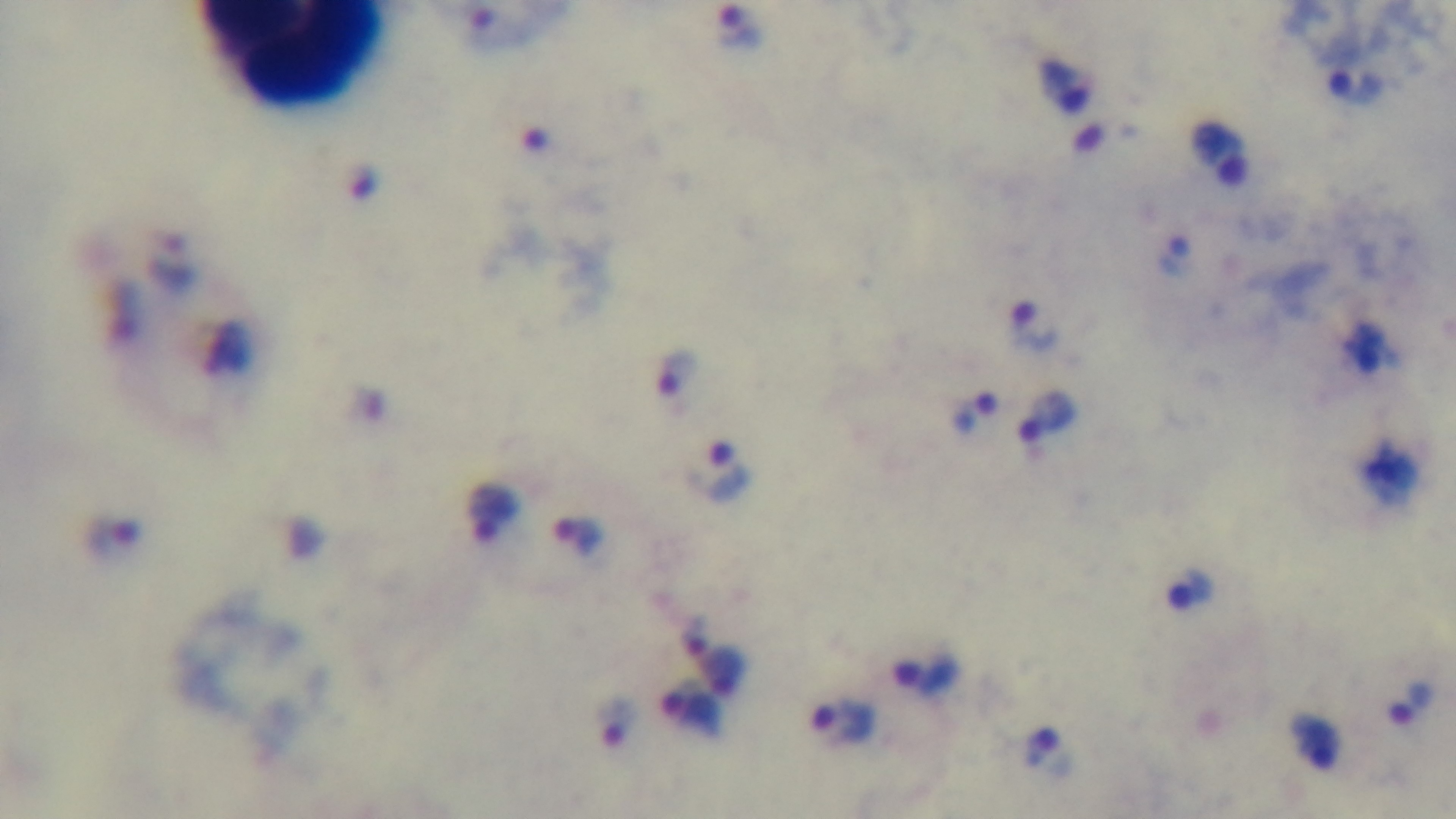
capture = mounted 4K digital camera
stain = Giemsa
preparation = thick smear
modality = light microscopy
objective = 100x oil immersion
field of view = one from the slide
malaria status = infected